Locate platelets.
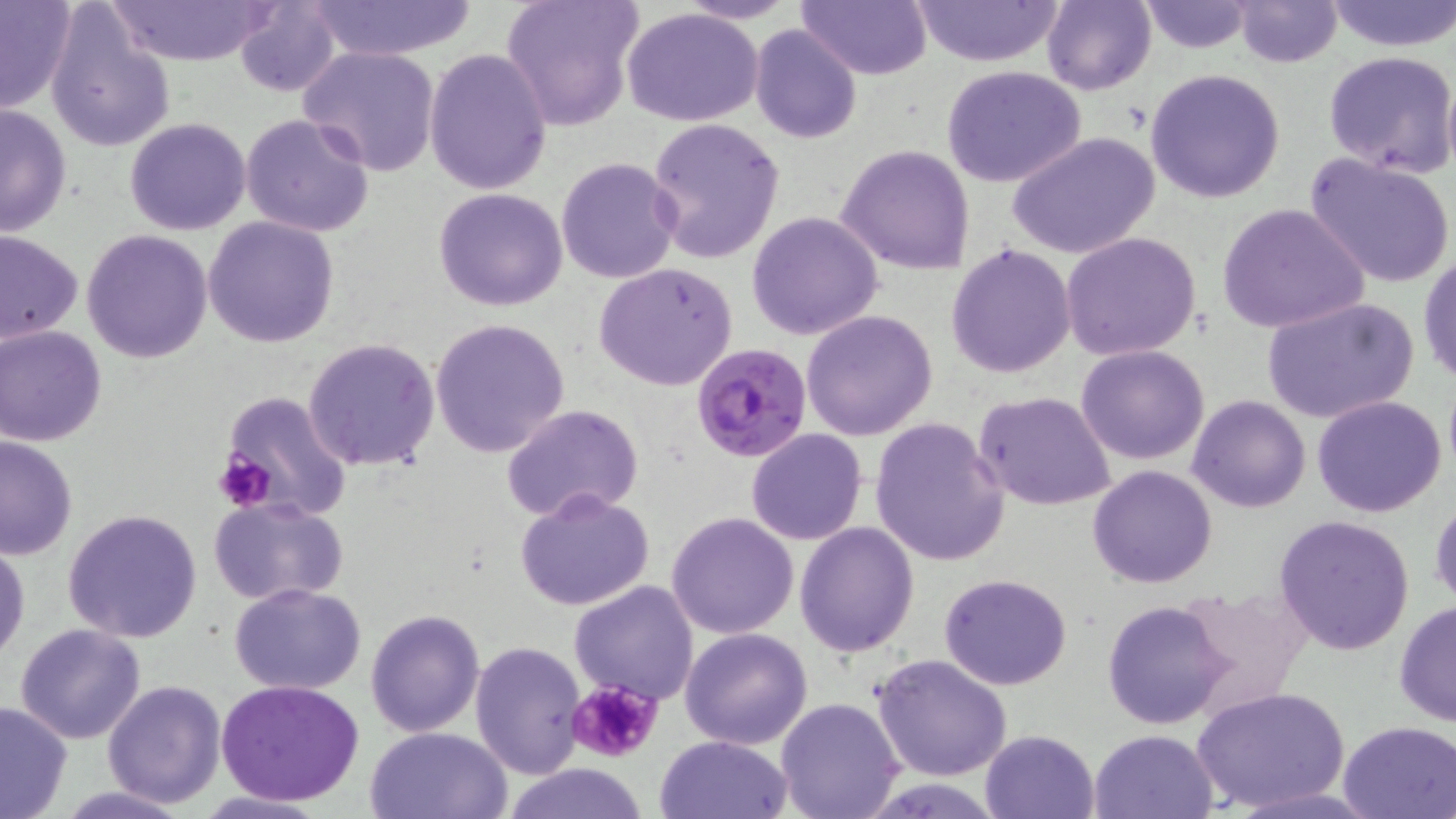

Approximate bounding boxes as (x1,y1)-(x2,y2) corner pairs in pixels.
Platelets: (212,449)-(275,511), (566,679)-(662,764).

Summary:
  - Uninfected red blood cell locations: (101,0)-(273,65), (304,0)-(477,61), (499,0)-(642,133), (679,0)-(802,24), (800,0)-(931,81), (910,0)-(1065,66), (1139,0)-(1258,53), (1327,0)-(1456,51), (0,1)-(77,113), (233,1)-(342,97), (1042,1)-(1157,96), (1233,1)-(1342,68), (43,5)-(176,155), (621,7)-(763,126), (750,25)-(862,146), (299,44)-(442,177), (1323,48)-(1456,179), (424,49)-(551,194), (942,66)-(1088,188), (1146,68)-(1286,204), (0,103)-(73,238), (241,113)-(375,238), (124,117)-(251,236), (646,117)-(785,265), (1008,131)-(1161,261), (836,144)-(975,276), (1304,152)-(1456,290), (556,157)-(682,285), (432,188)-(570,311), (1216,202)-(1370,334), (747,211)-(882,340), (203,217)-(339,347), (81,228)-(215,363), (0,230)-(83,346), (1060,231)-(1203,360), (945,243)-(1078,378), (1417,250)-(1456,387), (595,263)-(738,390), (1262,297)-(1418,426), (802,310)-(937,441), (429,316)-(571,458), (1,324)-(110,446), (302,337)-(442,472), (1076,344)-(1209,465), (1443,371)-(1456,487), (972,389)-(1117,513), (210,393)-(351,519), (1186,394)-(1311,513), (1311,396)-(1448,518), (500,403)-(645,523), (869,418)-(1010,567), (746,429)-(867,546), (0,434)-(78,560), (1088,464)-(1218,588), (515,488)-(656,610), (208,496)-(350,605), (1431,496)-(1455,609), (62,509)-(203,644), (666,512)-(799,640), (1274,514)-(1417,656), (794,522)-(919,658), (1,540)-(29,664), (939,572)-(1072,690), (569,580)-(699,703), (229,583)-(367,695), (1173,585)-(1313,720), (1393,599)-(1456,728), (1101,601)-(1233,728), (365,609)-(484,737), (14,623)-(147,744), (681,627)-(813,749), (470,640)-(587,778), (871,653)-(1013,782), (217,678)-(368,808), (102,679)-(228,808), (1191,686)-(1350,814), (774,697)-(905,819), (0,699)-(75,819), (1336,719)-(1456,819), (364,726)-(511,819), (980,728)-(1099,818), (1088,728)-(1217,818), (653,734)-(792,818), (500,763)-(650,819), (51,786)-(196,818)
  - Plasmodium falciparum-infected red blood cell locations: (690,343)-(813,463)
  - Slide-level diagnosis: Plasmodium falciparum
  - Field of view: single
  - Preparation: thin blood film
  - Image size: 1456×819 pixels
  - Stain: May-Grünwald-Giemsa
  - Magnification: 1000x
  - Modality: optical microscopy